Locate and identify every blood parasite.
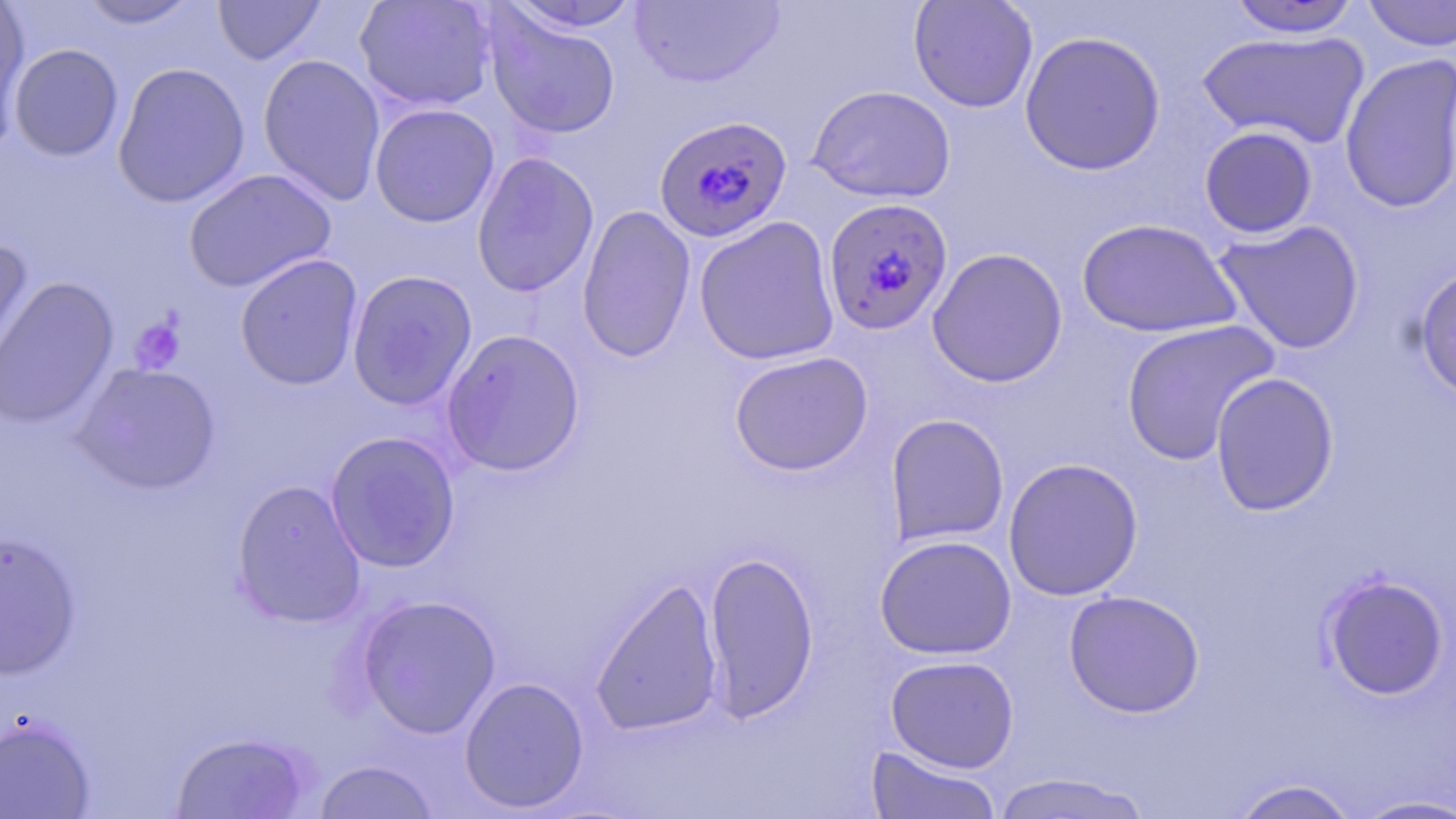
Approximate bounding boxes as named x1/y1/x2/y2 corners in pixels.
Plasmodium falciparum-infected red blood cells: (x1=654, y1=115, x2=794, y2=243), (x1=822, y1=197, x2=954, y2=336).
No Plasmodium ovale, Plasmodium malariae, Plasmodium vivax, Babesia divergens, or Trypanosoma brucei observed.

slide_level_diagnosis: Plasmodium falciparum
field_of_view: one of a larger specimen
preparation: thin blood film
image_size: 1456×819 pixels
stain: May-Grünwald-Giemsa
modality: light microscopy
magnification: 1000x
uninfected_red_blood_cell_locations: 'approximate bounding boxes as named x1/y1/x2/y2 corners in pixels: (x1=74, y1=0, x2=206, y2=30), (x1=212, y1=0, x2=326, y2=65), (x1=354, y1=0, x2=496, y2=112), (x1=629, y1=0, x2=785, y2=89), (x1=908, y1=0, x2=1038, y2=113), (x1=1360, y1=0, x2=1456, y2=52), (x1=501, y1=1, x2=644, y2=35), (x1=1226, y1=1, x2=1363, y2=38), (x1=0, y1=6, x2=32, y2=149), (x1=484, y1=8, x2=621, y2=140), (x1=1019, y1=30, x2=1166, y2=176), (x1=1196, y1=30, x2=1370, y2=149), (x1=9, y1=43, x2=124, y2=162), (x1=1338, y1=53, x2=1456, y2=214), (x1=257, y1=54, x2=387, y2=207), (x1=112, y1=62, x2=251, y2=209), (x1=806, y1=84, x2=956, y2=204), (x1=369, y1=103, x2=500, y2=227), (x1=1199, y1=126, x2=1319, y2=238), (x1=471, y1=151, x2=600, y2=298), (x1=183, y1=168, x2=337, y2=293), (x1=576, y1=204, x2=696, y2=363), (x1=693, y1=216, x2=840, y2=366), (x1=1076, y1=218, x2=1241, y2=338), (x1=1212, y1=219, x2=1366, y2=354), (x1=0, y1=241, x2=35, y2=385), (x1=926, y1=247, x2=1069, y2=388), (x1=235, y1=253, x2=364, y2=390), (x1=1413, y1=265, x2=1456, y2=403), (x1=347, y1=269, x2=478, y2=411), (x1=0, y1=276, x2=119, y2=428), (x1=1121, y1=320, x2=1280, y2=465), (x1=441, y1=328, x2=586, y2=477), (x1=729, y1=351, x2=873, y2=476), (x1=71, y1=361, x2=222, y2=495), (x1=1210, y1=372, x2=1340, y2=516), (x1=885, y1=413, x2=1010, y2=547), (x1=324, y1=430, x2=461, y2=573), (x1=1002, y1=457, x2=1143, y2=601), (x1=231, y1=479, x2=367, y2=628), (x1=0, y1=531, x2=81, y2=680), (x1=874, y1=535, x2=1017, y2=660), (x1=703, y1=549, x2=819, y2=722), (x1=1318, y1=573, x2=1450, y2=701), (x1=590, y1=576, x2=724, y2=737), (x1=1063, y1=589, x2=1205, y2=718), (x1=355, y1=594, x2=502, y2=738), (x1=884, y1=655, x2=1020, y2=773), (x1=459, y1=676, x2=589, y2=813), (x1=0, y1=716, x2=95, y2=818), (x1=171, y1=731, x2=312, y2=818), (x1=864, y1=743, x2=1003, y2=818), (x1=312, y1=759, x2=440, y2=819), (x1=989, y1=772, x2=1154, y2=818), (x1=1228, y1=778, x2=1362, y2=819), (x1=1348, y1=794, x2=1456, y2=818)'
platelet_locations: 'approximate bounding boxes as named x1/y1/x2/y2 corners in pixels: (x1=128, y1=316, x2=185, y2=374)'